Assess this cell for malaria.
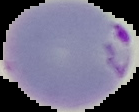

Parasitized.

Summary:
  - Image size: 139×112 pixels
  - Image type: segmented cell region on a black background
  - Preparation: thin blood film